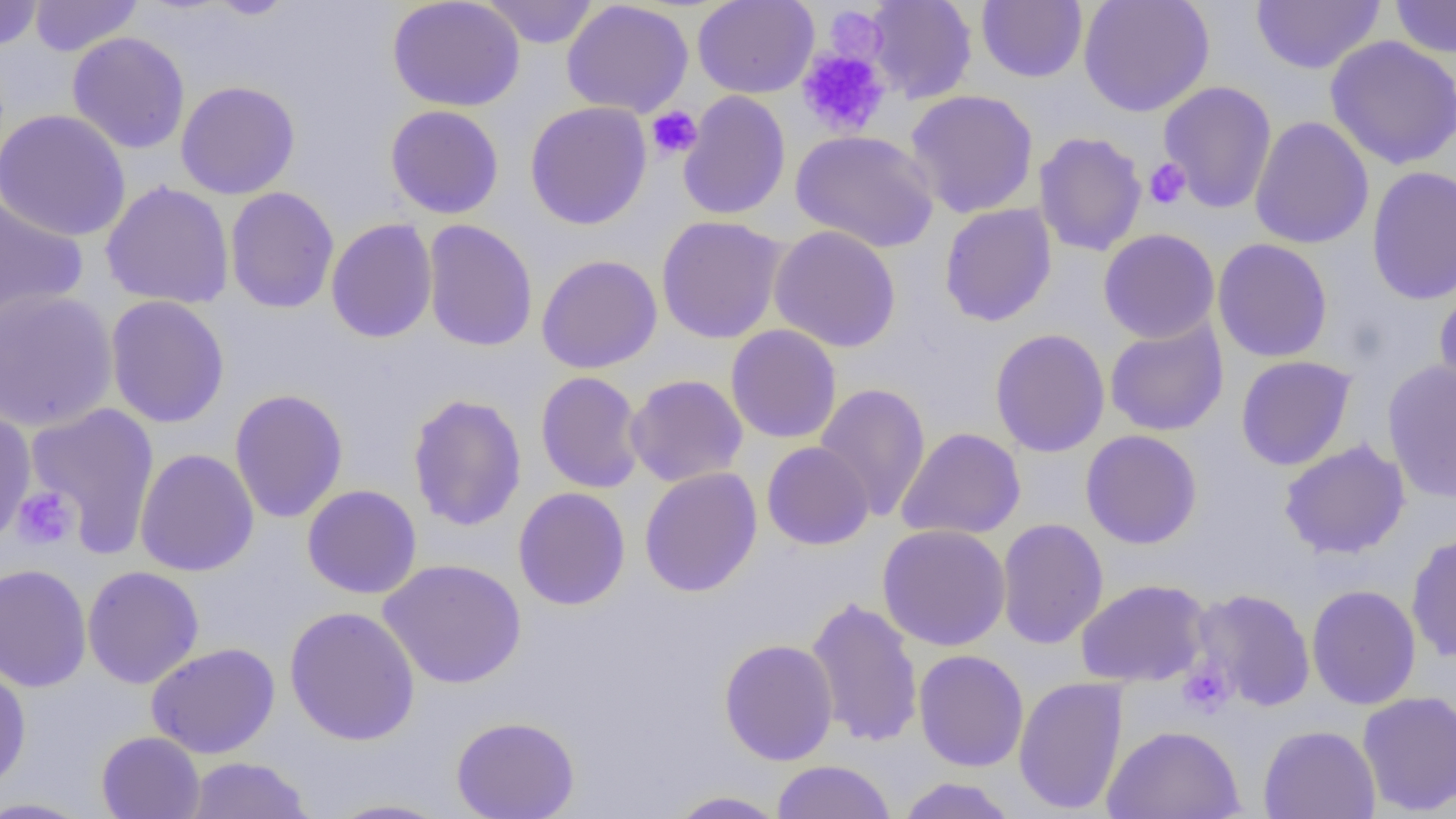

slide-level diagnosis = negative for blood parasites
magnification = 1000x
image size = 1456×819 pixels
field of view = single
platelet locations = approximate bounding boxes as (x1, y1, x2, y2) in pixels: (824, 6, 887, 64), (796, 47, 891, 138), (645, 106, 702, 159), (1143, 158, 1190, 210), (13, 487, 78, 550), (1177, 660, 1234, 717)
uninfected red blood cell locations = approximate bounding boxes as (x1, y1, x2, y2) in pixels: (0, 0, 45, 51), (29, 0, 143, 57), (205, 0, 297, 20), (388, 0, 526, 112), (481, 0, 599, 48), (561, 0, 694, 118), (692, 0, 819, 98), (864, 0, 978, 104), (1077, 0, 1215, 117), (1390, 0, 1456, 59), (977, 1, 1088, 83), (1250, 1, 1385, 74), (67, 32, 191, 154), (1324, 35, 1456, 171), (175, 80, 301, 199), (1158, 81, 1277, 213), (905, 89, 1039, 219), (678, 90, 791, 220), (524, 101, 652, 230), (385, 104, 504, 219), (0, 108, 131, 242), (1249, 116, 1374, 249), (791, 130, 939, 253), (1033, 131, 1147, 257), (1366, 165, 1456, 305), (100, 180, 235, 309), (224, 186, 340, 314), (0, 194, 88, 325), (938, 203, 1057, 327), (655, 215, 787, 344), (325, 218, 438, 343), (422, 219, 538, 352), (769, 224, 902, 353), (1098, 228, 1220, 344), (1213, 238, 1332, 362), (536, 253, 663, 373), (1434, 286, 1456, 409), (0, 289, 117, 431), (105, 295, 230, 429), (1104, 318, 1229, 436), (726, 324, 842, 444), (989, 328, 1110, 458), (1235, 355, 1356, 471), (1382, 359, 1456, 503), (535, 371, 646, 493), (625, 374, 749, 487), (815, 382, 931, 521), (230, 389, 348, 523), (407, 393, 527, 532), (24, 402, 161, 556), (0, 407, 37, 546), (896, 427, 1026, 540), (1081, 430, 1202, 549), (1278, 439, 1410, 559), (761, 441, 874, 550), (134, 448, 259, 576), (639, 467, 762, 597), (302, 484, 422, 599), (513, 486, 631, 611), (996, 517, 1108, 649), (877, 523, 1011, 651), (1405, 532, 1456, 662), (378, 559, 527, 689), (0, 563, 92, 692), (82, 565, 204, 689), (1075, 579, 1211, 687), (1307, 584, 1421, 710), (1191, 587, 1316, 712), (805, 596, 924, 748), (284, 606, 420, 746), (719, 638, 839, 766), (146, 642, 281, 759), (914, 649, 1029, 772), (0, 662, 31, 793), (1013, 676, 1128, 815), (1357, 690, 1456, 815), (451, 715, 581, 818), (1258, 724, 1380, 819), (1103, 725, 1245, 819), (96, 731, 206, 819), (184, 757, 314, 818), (770, 760, 896, 819), (897, 776, 1017, 819), (665, 790, 790, 818), (0, 796, 96, 818), (324, 798, 454, 818)
preparation = thin blood smear
modality = optical microscopy